Locate every blood parasite and identify its species.
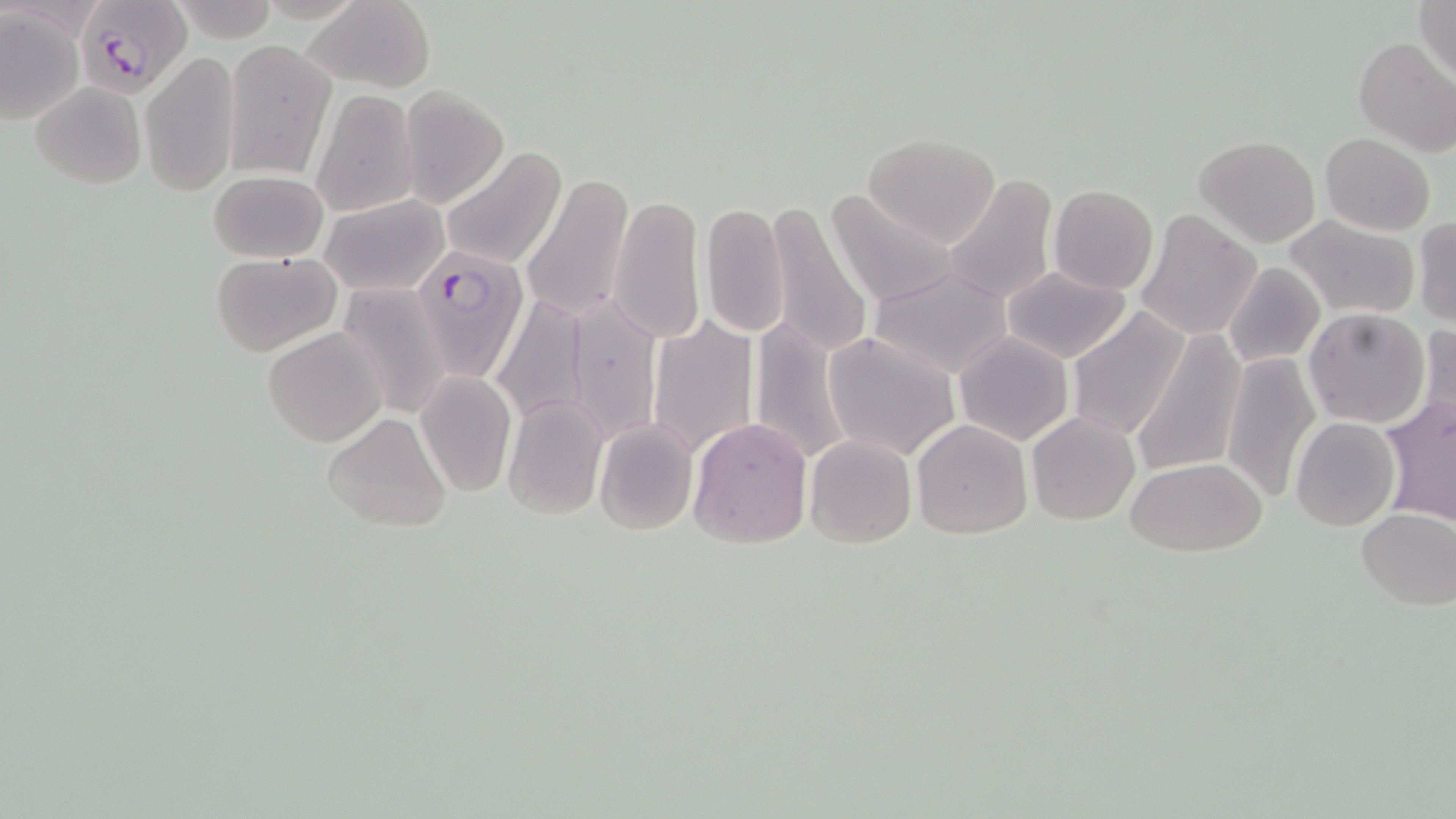

Approximate bounding boxes as named x1/y1/x2/y2 corners in pixels.
Plasmodium falciparum-infected red blood cells: (x1=81, y1=0, x2=192, y2=97), (x1=410, y1=246, x2=530, y2=378).
No Plasmodium ovale, Plasmodium malariae, Plasmodium vivax, Babesia divergens, or Trypanosoma brucei observed.

Uninfected red blood cell locations: (x1=1415, y1=0, x2=1456, y2=87), (x1=170, y1=1, x2=280, y2=44), (x1=304, y1=1, x2=436, y2=92), (x1=0, y1=9, x2=85, y2=123), (x1=1353, y1=37, x2=1455, y2=157), (x1=223, y1=39, x2=335, y2=179), (x1=140, y1=50, x2=240, y2=199), (x1=30, y1=81, x2=146, y2=189), (x1=399, y1=85, x2=510, y2=210), (x1=307, y1=90, x2=418, y2=215), (x1=1320, y1=133, x2=1435, y2=236), (x1=863, y1=134, x2=1000, y2=247), (x1=1194, y1=135, x2=1320, y2=247), (x1=439, y1=147, x2=567, y2=269), (x1=208, y1=170, x2=328, y2=262), (x1=521, y1=173, x2=633, y2=321), (x1=941, y1=173, x2=1059, y2=308), (x1=1048, y1=184, x2=1158, y2=295), (x1=827, y1=188, x2=960, y2=308), (x1=608, y1=193, x2=705, y2=346), (x1=321, y1=195, x2=448, y2=296), (x1=766, y1=201, x2=873, y2=360), (x1=700, y1=203, x2=788, y2=338), (x1=1135, y1=210, x2=1262, y2=340), (x1=1284, y1=216, x2=1420, y2=319), (x1=1412, y1=217, x2=1456, y2=327), (x1=212, y1=251, x2=342, y2=356), (x1=1222, y1=263, x2=1325, y2=368), (x1=867, y1=267, x2=1014, y2=378), (x1=1000, y1=267, x2=1132, y2=362), (x1=335, y1=284, x2=453, y2=419), (x1=489, y1=292, x2=593, y2=426), (x1=563, y1=294, x2=661, y2=442), (x1=1065, y1=306, x2=1191, y2=443), (x1=1303, y1=307, x2=1430, y2=428), (x1=647, y1=314, x2=760, y2=461), (x1=749, y1=315, x2=855, y2=467), (x1=1416, y1=322, x2=1455, y2=433), (x1=262, y1=326, x2=387, y2=448), (x1=953, y1=331, x2=1073, y2=446), (x1=823, y1=332, x2=961, y2=461), (x1=1132, y1=332, x2=1247, y2=477), (x1=1220, y1=350, x2=1321, y2=504), (x1=414, y1=370, x2=519, y2=497), (x1=500, y1=395, x2=609, y2=519), (x1=1380, y1=395, x2=1456, y2=526), (x1=322, y1=412, x2=454, y2=532), (x1=1027, y1=412, x2=1140, y2=525), (x1=687, y1=416, x2=814, y2=548), (x1=1291, y1=418, x2=1400, y2=531), (x1=912, y1=419, x2=1033, y2=539), (x1=594, y1=421, x2=698, y2=535), (x1=804, y1=434, x2=917, y2=548), (x1=1125, y1=457, x2=1267, y2=556), (x1=1355, y1=508, x2=1454, y2=609). Slide-level diagnosis: Plasmodium falciparum. Optical microscopy. Thin blood film. Image is 1456×819 pixels. Captured at 1000x magnification. May-Grünwald-Giemsa stain. Single field of view.